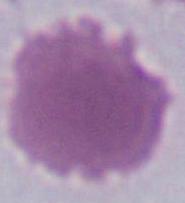

{
  "modality": "photomicrograph",
  "identification": "red blood cell",
  "magnification": "1000x"
}